Describe the morphology of the red blood cells.
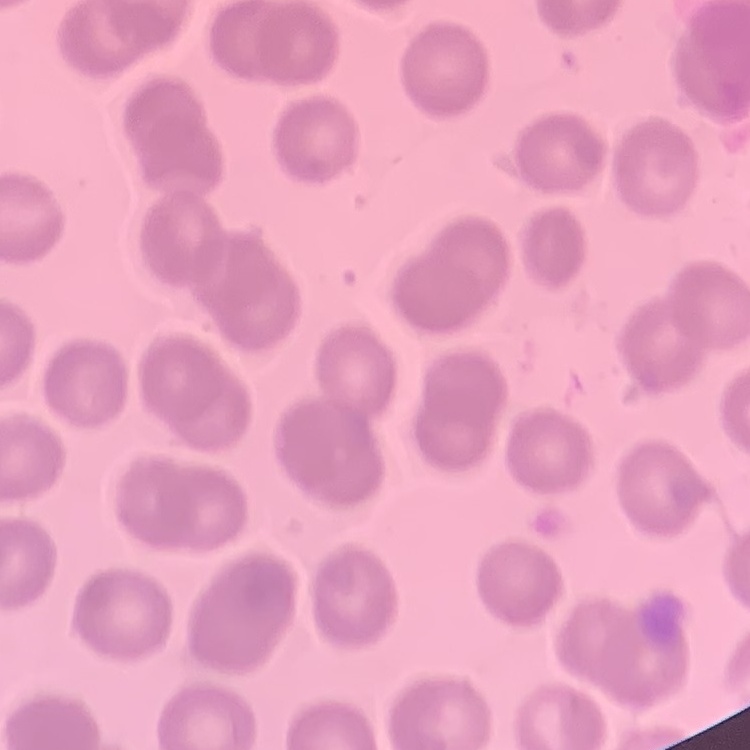

They show no rouleaux formation.

stain = Field's or Giemsa
preparation = thin peripheral smear
image type = square crop of a larger photomicrograph